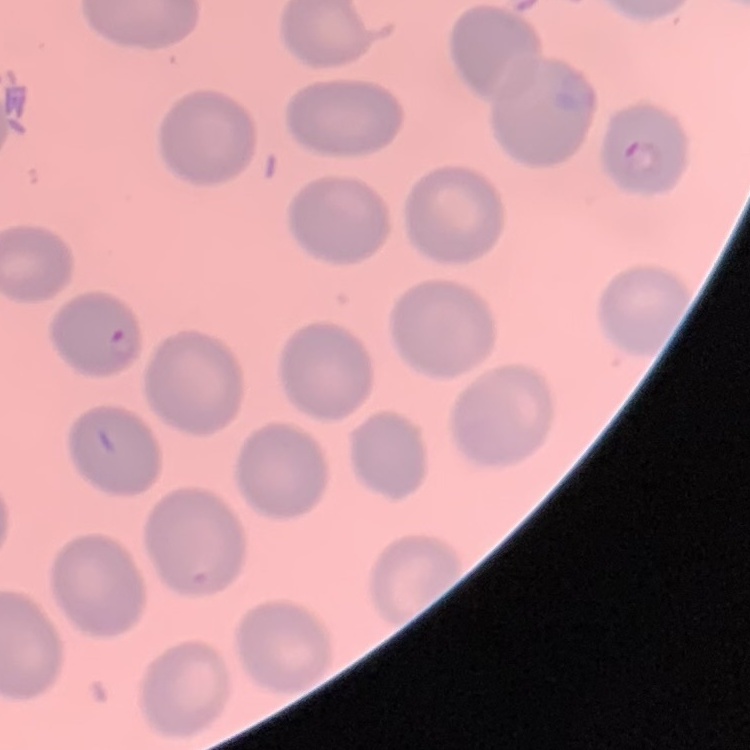

The erythrocytes exhibit no rouleaux formation. One tile cut from a larger photomicrograph. Field's or Giemsa stain. Thin peripheral smear.